Assess the morphology of the erythrocytes.
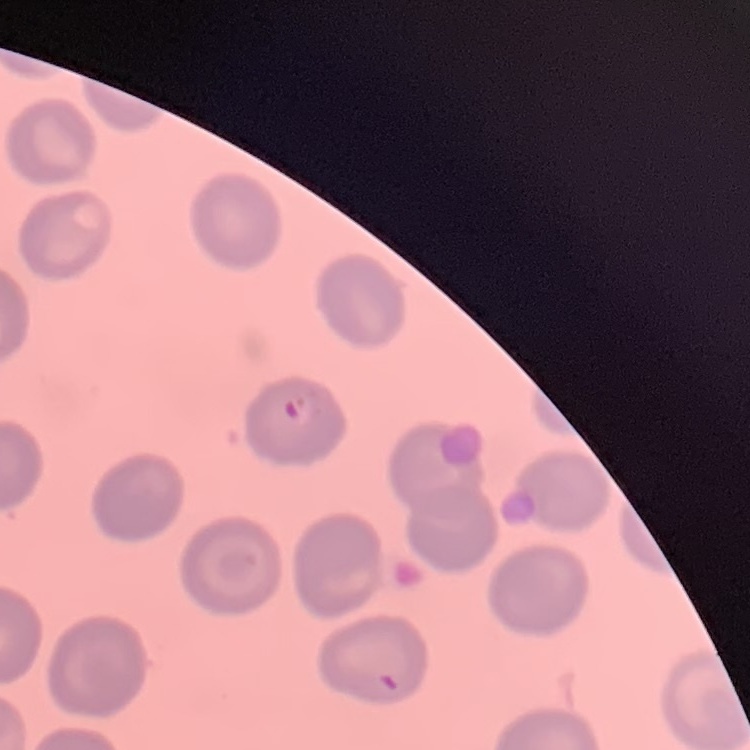

No rouleaux formation.

Summary:
  - Preparation: thin peripheral smear
  - Stain: Field's or Giemsa
  - Image type: square crop of a larger photomicrograph